Identify the parasite.
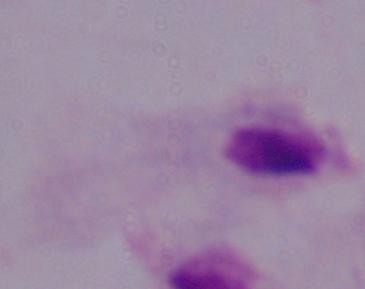

This is a trichomonad.

modality = photomicrograph
magnification = 1000x